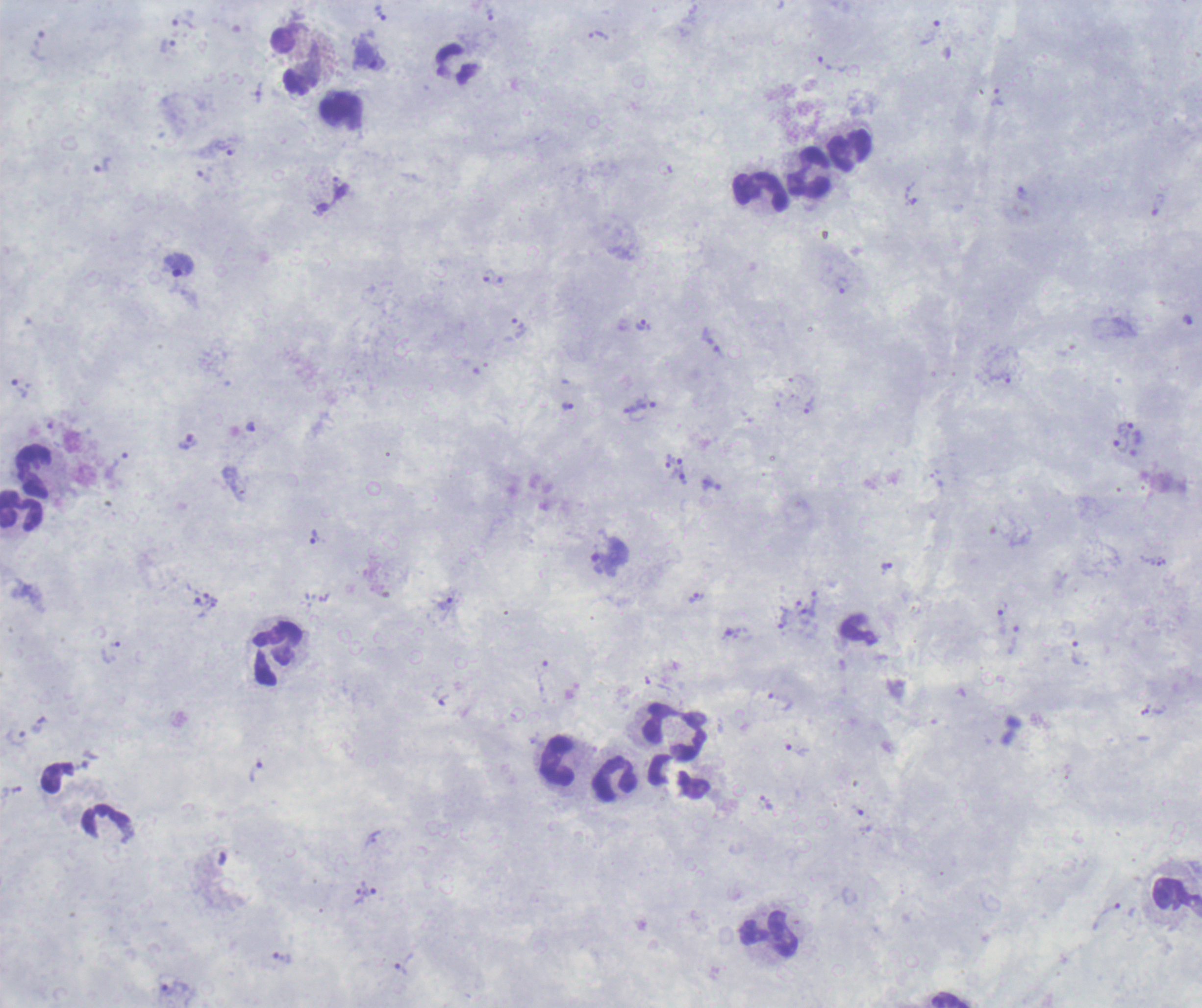 Thick blood film. Image is 1202×1008 pixels. Romanowsky-stained preparation. One field from this slide.